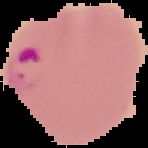 Result: Plasmodium parasites detected. Image is 148×148 pixels. Cell region segmented out of the field of view; the surrounding area is masked to black. From a thin blood film.